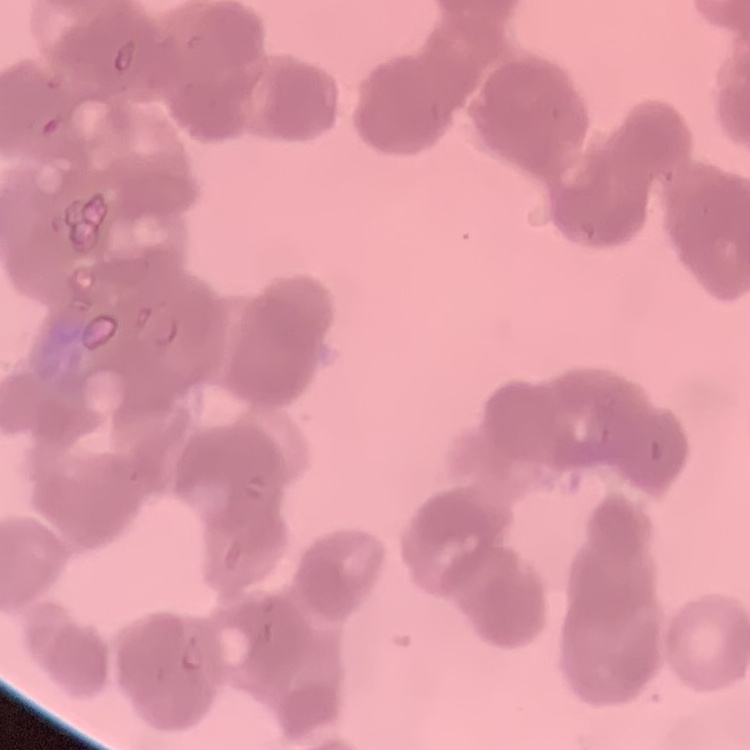

Summary:
  - Red blood cell morphology: rouleaux formation
  - Image type: one tile cut from a larger photomicrograph
  - Stain: Field's or Giemsa
  - Preparation: thin peripheral smear